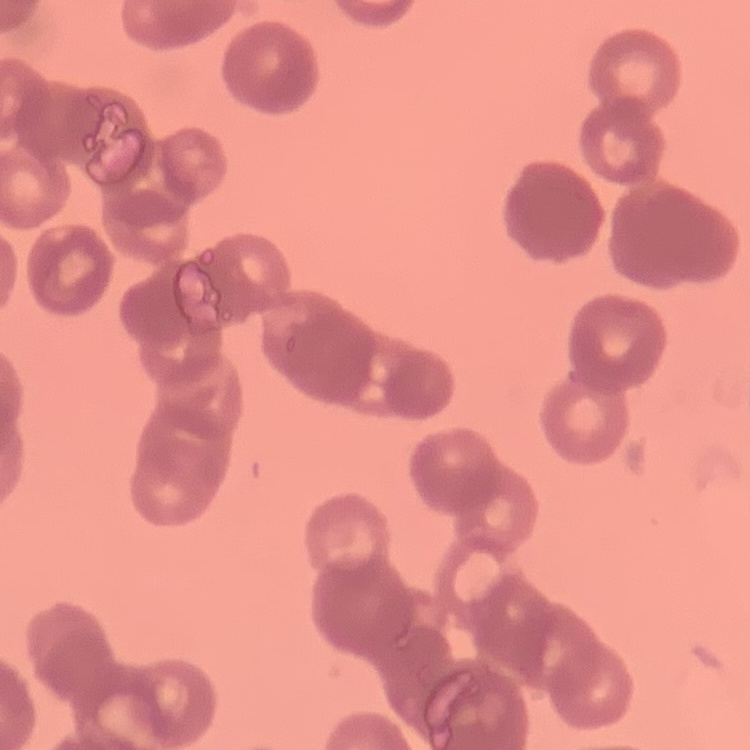

The red blood cells exhibit rouleaux formation. Stained with either Field's or Giemsa. Thin blood smear. One tile cut from a larger photomicrograph.